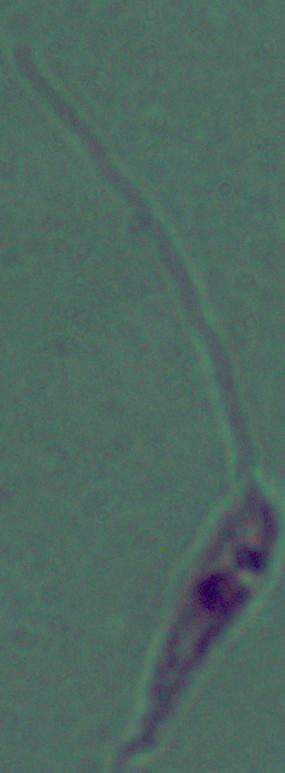

A Leishmania parasite is seen. Captured at 1000x magnification. Micrograph.